Outline every parasitised red blood cell.
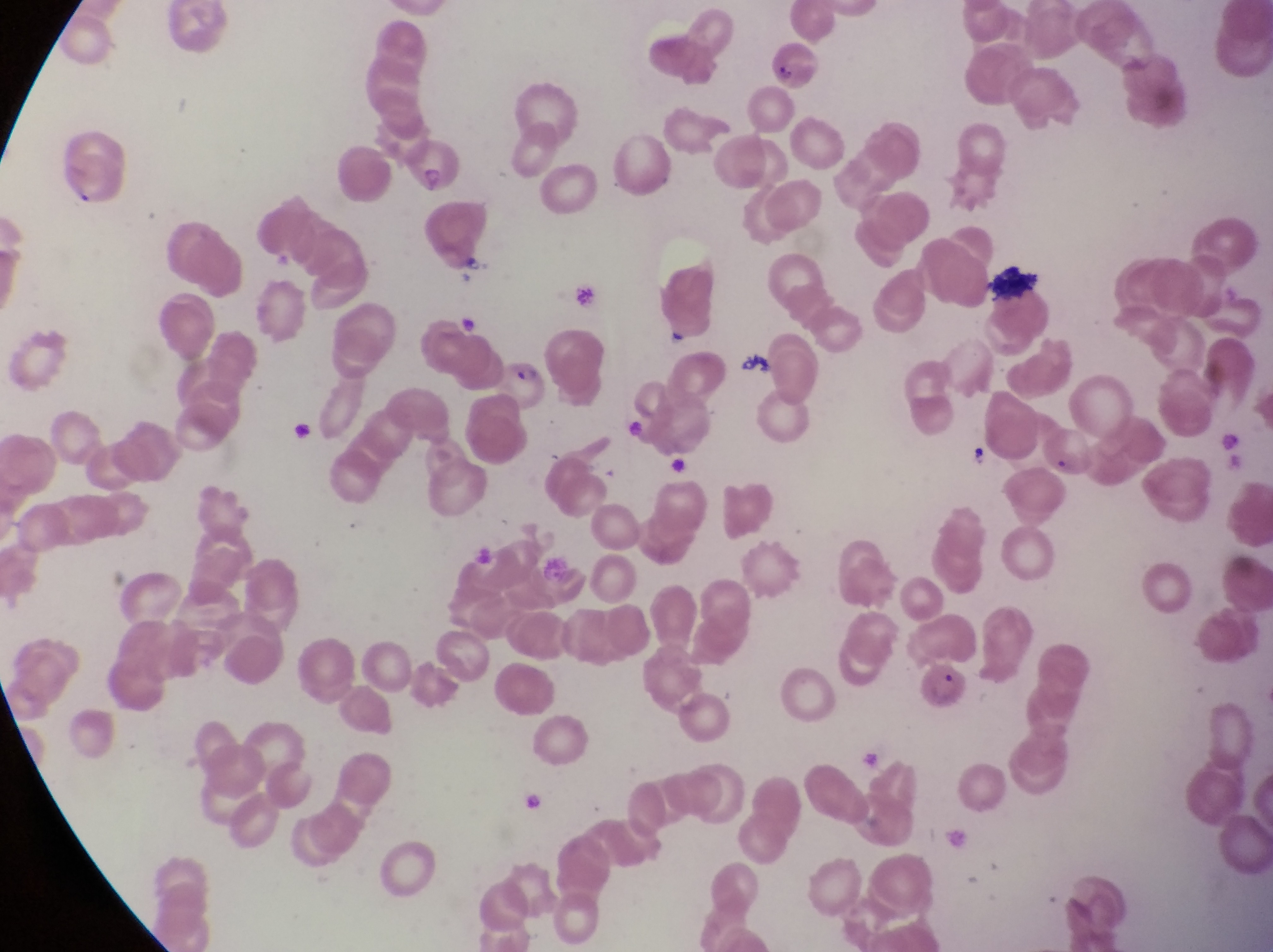
Approximate bounding boxes as [left, top, right, bottom] in pixels.
Parasitised red blood cells: [400, 139, 463, 196], [491, 352, 549, 412], [916, 657, 974, 714].

artifact (platelet-like body, stain precipitate, or debris) locations = approximate bounding boxes as [left, top, right, bottom] in pixels: [991, 258, 1049, 303], [963, 435, 1000, 468]
preparation = thin blood smear
capture = smartphone photograph through the eyepiece of an Olympus CX-23 microscope
magnification = 1000x
field of view = single
image size = 1273×952 pixels
country = Uganda